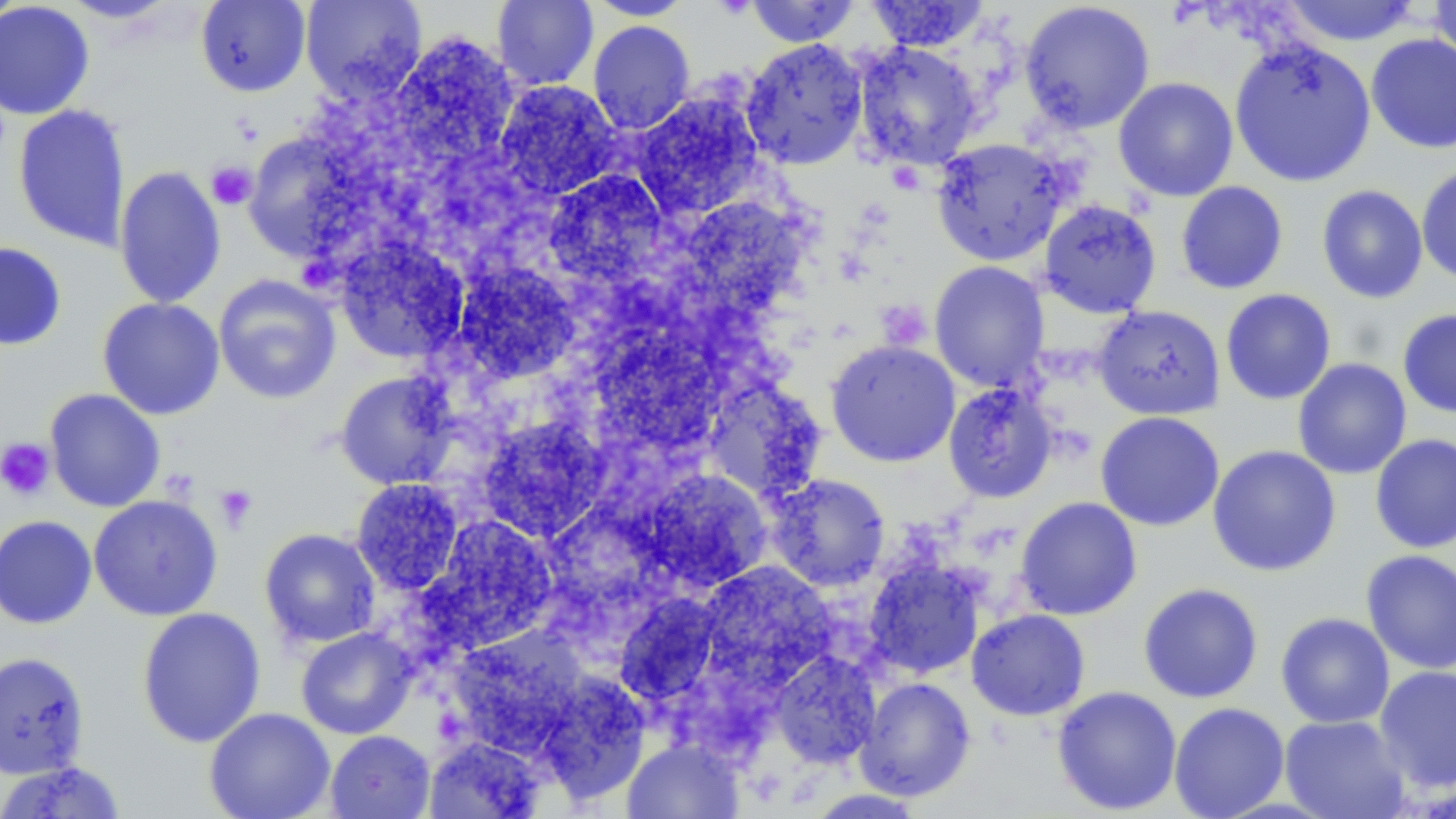
Approximate bounding boxes as named x1/y1/x2/y2 corners in pixels. Uninfected red blood cell locations: (x1=0, y1=0, x2=25, y2=30), (x1=59, y1=0, x2=181, y2=24), (x1=195, y1=0, x2=311, y2=97), (x1=300, y1=0, x2=427, y2=102), (x1=491, y1=0, x2=599, y2=91), (x1=585, y1=0, x2=697, y2=20), (x1=744, y1=0, x2=860, y2=47), (x1=864, y1=0, x2=990, y2=51), (x1=1276, y1=0, x2=1425, y2=46), (x1=1428, y1=0, x2=1456, y2=74), (x1=0, y1=1, x2=94, y2=120), (x1=1018, y1=1, x2=1156, y2=133), (x1=588, y1=20, x2=695, y2=135), (x1=383, y1=34, x2=519, y2=173), (x1=1365, y1=34, x2=1456, y2=154), (x1=741, y1=38, x2=868, y2=169), (x1=1229, y1=38, x2=1377, y2=188), (x1=851, y1=42, x2=984, y2=170), (x1=1113, y1=77, x2=1239, y2=201), (x1=494, y1=80, x2=620, y2=200), (x1=631, y1=92, x2=764, y2=219), (x1=12, y1=103, x2=131, y2=252), (x1=930, y1=137, x2=1071, y2=266), (x1=247, y1=141, x2=373, y2=258), (x1=1416, y1=163, x2=1456, y2=286), (x1=114, y1=165, x2=227, y2=309), (x1=544, y1=171, x2=668, y2=288), (x1=1176, y1=181, x2=1288, y2=295), (x1=1316, y1=185, x2=1429, y2=304), (x1=686, y1=199, x2=807, y2=305), (x1=1038, y1=199, x2=1162, y2=319), (x1=335, y1=238, x2=469, y2=364), (x1=0, y1=241, x2=67, y2=351), (x1=929, y1=261, x2=1050, y2=392), (x1=453, y1=263, x2=580, y2=383), (x1=213, y1=274, x2=341, y2=405), (x1=1220, y1=288, x2=1337, y2=405), (x1=97, y1=297, x2=225, y2=420), (x1=1094, y1=304, x2=1225, y2=420), (x1=1397, y1=309, x2=1456, y2=418), (x1=599, y1=325, x2=719, y2=455), (x1=826, y1=340, x2=960, y2=467), (x1=1292, y1=358, x2=1412, y2=479), (x1=334, y1=371, x2=459, y2=490), (x1=712, y1=379, x2=816, y2=497), (x1=942, y1=383, x2=1058, y2=503), (x1=44, y1=388, x2=165, y2=512), (x1=1095, y1=411, x2=1224, y2=531), (x1=476, y1=416, x2=609, y2=542), (x1=1369, y1=433, x2=1456, y2=554), (x1=1207, y1=444, x2=1341, y2=577), (x1=639, y1=468, x2=774, y2=592), (x1=765, y1=473, x2=890, y2=591), (x1=351, y1=479, x2=464, y2=596), (x1=88, y1=494, x2=223, y2=621), (x1=1015, y1=496, x2=1142, y2=620), (x1=0, y1=515, x2=98, y2=629), (x1=418, y1=515, x2=559, y2=651), (x1=259, y1=528, x2=381, y2=648), (x1=1361, y1=549, x2=1456, y2=674), (x1=864, y1=558, x2=985, y2=679), (x1=697, y1=562, x2=836, y2=688), (x1=1138, y1=583, x2=1263, y2=704), (x1=614, y1=593, x2=722, y2=708), (x1=136, y1=607, x2=266, y2=748), (x1=966, y1=608, x2=1090, y2=720), (x1=1276, y1=612, x2=1395, y2=728), (x1=447, y1=627, x2=586, y2=757), (x1=296, y1=628, x2=416, y2=739), (x1=0, y1=650, x2=90, y2=780), (x1=769, y1=650, x2=881, y2=769), (x1=1374, y1=665, x2=1456, y2=793), (x1=535, y1=675, x2=650, y2=804), (x1=855, y1=677, x2=976, y2=801), (x1=1052, y1=685, x2=1182, y2=815), (x1=1169, y1=702, x2=1290, y2=819), (x1=204, y1=707, x2=335, y2=819), (x1=1279, y1=714, x2=1410, y2=819), (x1=325, y1=730, x2=435, y2=819), (x1=424, y1=736, x2=545, y2=818), (x1=622, y1=738, x2=744, y2=819), (x1=0, y1=760, x2=127, y2=818), (x1=803, y1=788, x2=930, y2=818). Platelet locations: (x1=207, y1=162, x2=257, y2=210), (x1=0, y1=438, x2=55, y2=501), (x1=214, y1=484, x2=258, y2=532). Slide-level diagnosis: no evidence of blood parasites. Image is 1456×819 pixels. Captured at 1000x magnification. May-Grünwald-Giemsa-stained preparation. Optical microscopy. One field of a larger specimen. Thin blood smear.